Name the parasite shown.
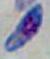

Toxoplasma gondii.

magnification = 1000x
modality = micrograph